Assess this cell for malaria.
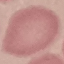
It is uninfected.

stain = Giemsa
capture = smartphone camera at the microscope eyepiece
image type = automatically extracted cell patch, resized to 64 × 64 pixels
preparation = thin smear